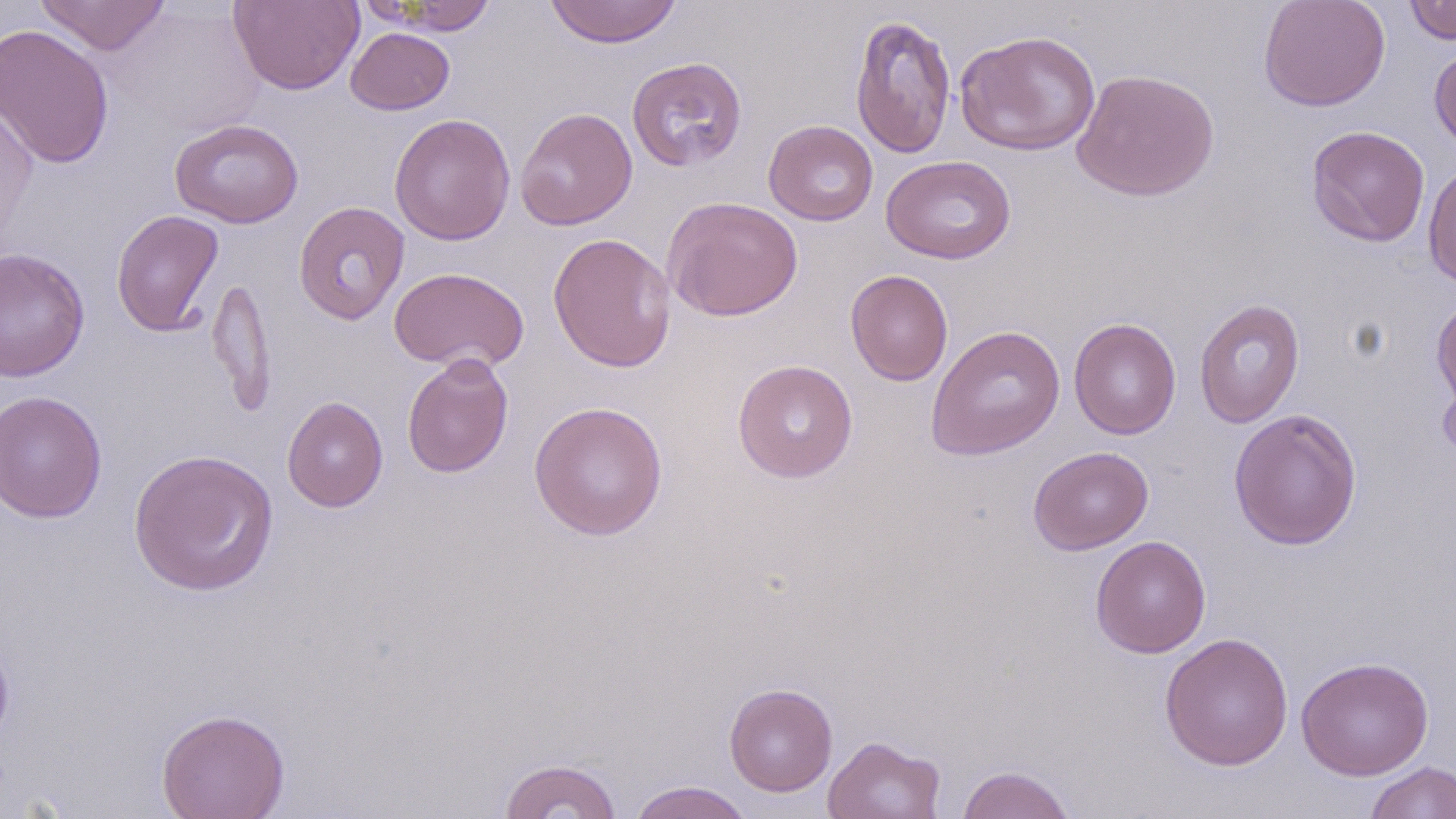
Summary:
  - Coordinate format: approximate bounding boxes as [x1, y1, x2, y2] in pixels
  - Uninfected red blood cell locations: [36, 0, 172, 56], [365, 0, 500, 35], [545, 0, 682, 48], [1258, 0, 1391, 112], [1403, 0, 1456, 45], [228, 1, 364, 95], [111, 2, 264, 139], [850, 13, 956, 159], [0, 23, 115, 170], [345, 27, 455, 115], [955, 29, 1101, 157], [1428, 42, 1456, 155], [626, 57, 747, 171], [1071, 68, 1221, 202], [0, 97, 38, 254], [515, 107, 638, 230], [388, 113, 516, 246], [169, 118, 304, 228], [763, 120, 878, 225], [1305, 125, 1430, 247], [880, 155, 1016, 264], [1422, 162, 1456, 290], [662, 196, 803, 321], [293, 201, 410, 325], [111, 209, 224, 338], [548, 232, 677, 373], [0, 247, 90, 382], [389, 266, 529, 373], [845, 269, 953, 386], [206, 276, 276, 416], [1431, 297, 1456, 414], [1194, 298, 1306, 428], [1068, 317, 1180, 439], [926, 324, 1066, 461], [401, 354, 514, 479], [732, 359, 858, 482], [1437, 361, 1456, 466], [0, 390, 107, 523], [282, 396, 388, 513], [529, 401, 668, 541], [1228, 408, 1363, 550], [1028, 446, 1154, 554], [128, 448, 280, 596], [1090, 535, 1212, 658], [1159, 632, 1294, 771], [1296, 656, 1434, 780], [724, 682, 838, 796], [155, 708, 290, 819], [822, 735, 946, 819], [498, 757, 623, 819], [1363, 761, 1456, 819], [955, 764, 1077, 819], [627, 781, 756, 819]
  - Slide-level diagnosis: no evidence of blood parasites
  - Stain: May-Grünwald-Giemsa
  - Image size: 1456×819 pixels
  - Preparation: thin blood smear
  - Modality: light microscopy
  - Magnification: 1000x
  - Field of view: single